Look for Plasmodium parasites.
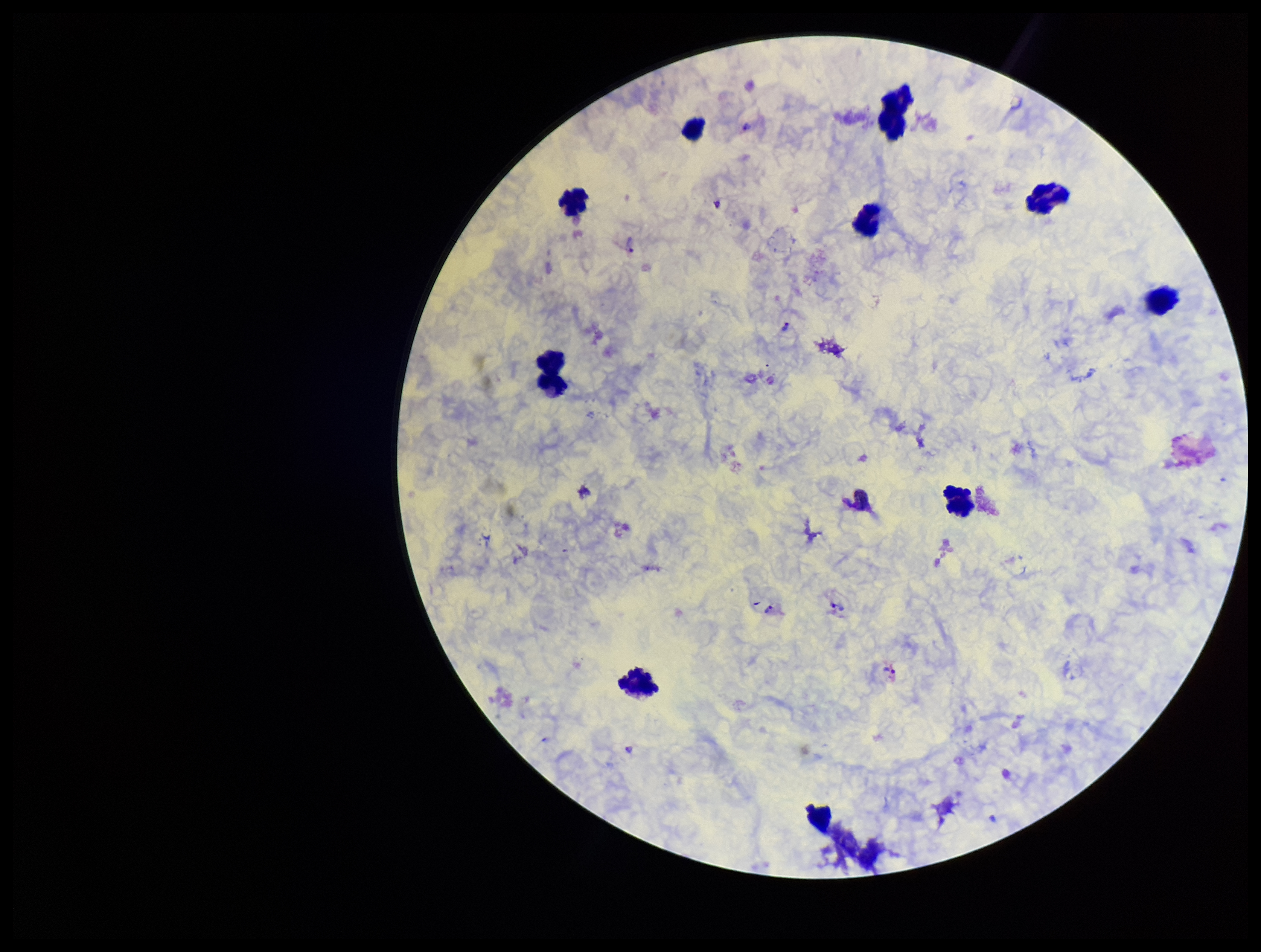

Detected.

Preparation: thick. Leukocyte count: 10. Patient malaria status: infected. Photographed through the microscope eyepiece with a smartphone camera. Image is 1261×952 pixels. One field from this slide. Parasite count: 6. Species reported for this patient: Plasmodium vivax. Giemsa stain.